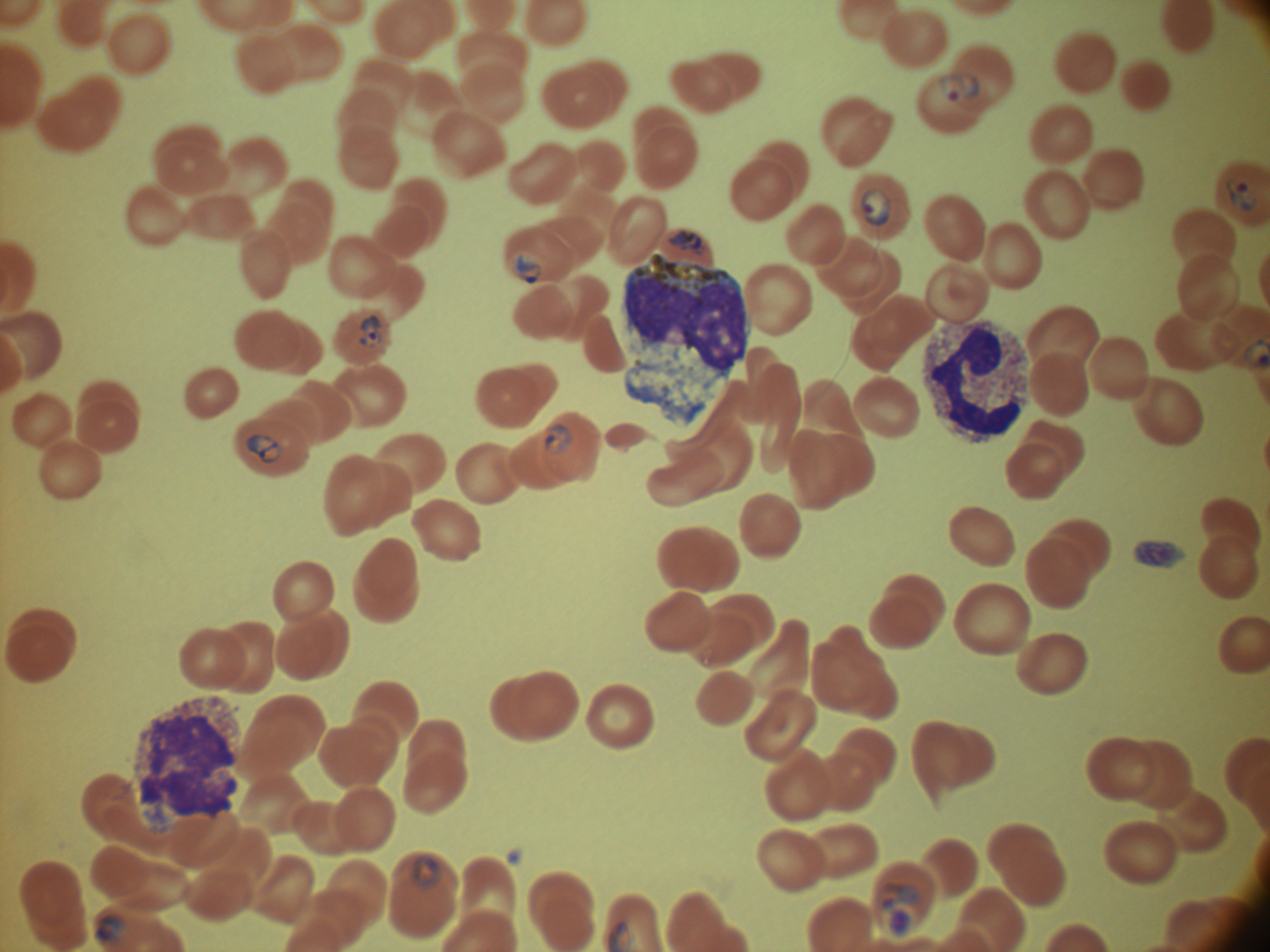 Approximate bounding boxes as (x1,y1)-(x2,y2) corner pairs in pixels, from the source annotation, which is not necessarily exhaustive. Trophozoite locations: (668,229)-(708,255), (879,883)-(922,937). Ring form locations: (937,71)-(980,103), (1224,180)-(1258,212), (861,188)-(891,226), (511,251)-(545,283), (359,314)-(383,349), (545,424)-(571,453), (244,434)-(283,463), (411,856)-(440,889), (95,914)-(125,943). Life-cycle stages among the annotated parasites: ring form, trophozoite. One field from this slide. Leica DM2000 optical microscope with a built-in camera. Image is 1270×952 pixels. Giemsa stain. Thin blood smear. Captured at 100x magnification. Species: Plasmodium falciparum.